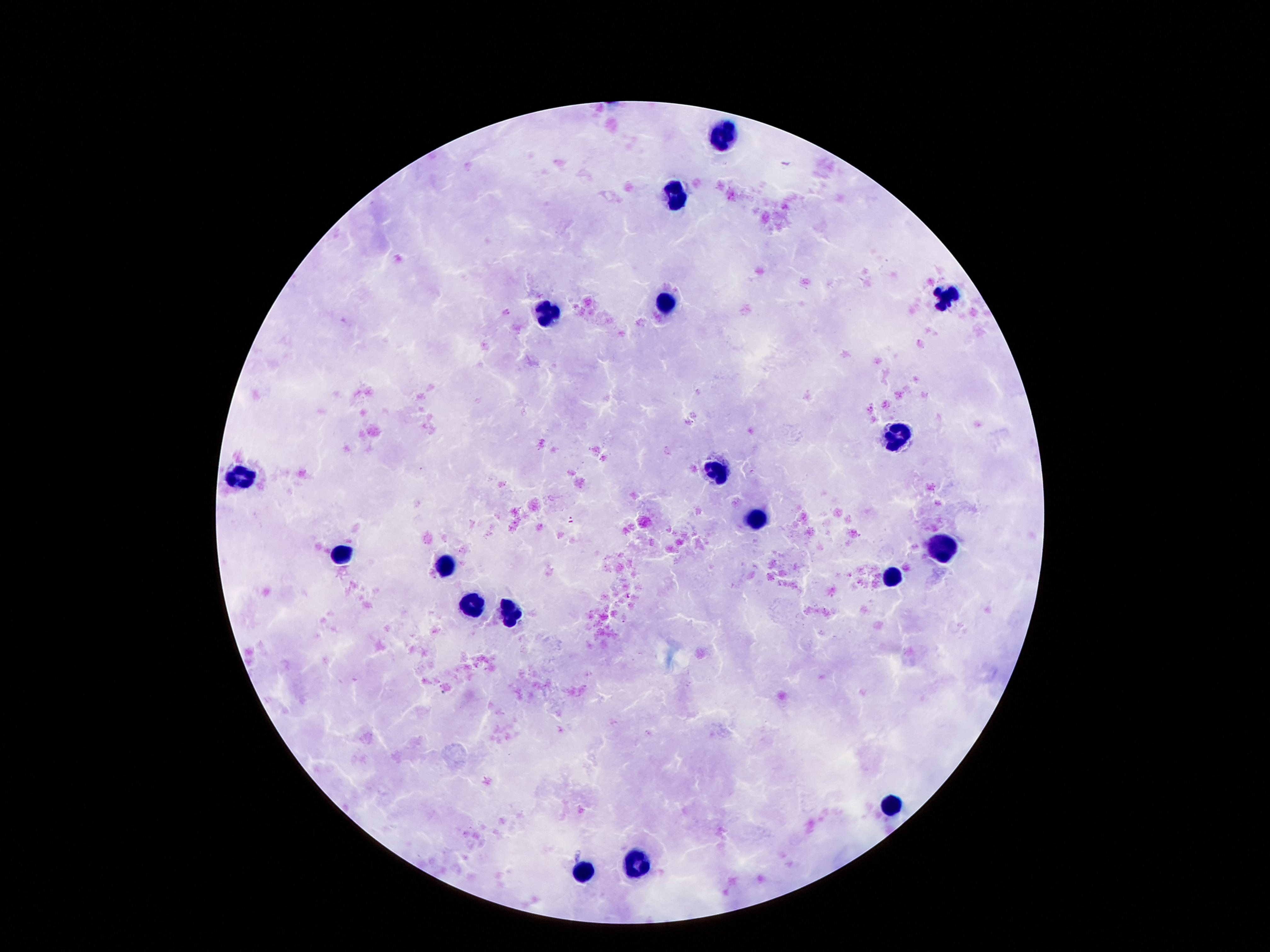
Approximate centers as (x, y) in pixels.
Summary:
  - Leukocyte locations: (719, 131), (676, 191), (951, 298), (666, 300), (547, 313), (900, 434), (717, 468), (242, 478), (756, 521), (945, 550), (340, 558), (443, 567), (894, 578), (471, 606), (508, 613), (894, 804), (637, 862), (586, 871)
  - Patient malaria status: uninfected
  - Field of view: single
  - Stain: Giemsa
  - Preparation: thick blood film
  - Magnification: 100x
  - Image size: 1270×952 pixels
  - Capture: smartphone camera through the microscope eyepiece